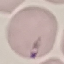

result = no malaria parasites seen
image type = cell patch, automatically extracted from a larger field of view and resized to 64 × 64 pixels
preparation = thin blood smear
capture = smartphone camera at the microscope eyepiece
stain = Giemsa